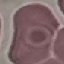
{
  "result": "no malaria parasites detected",
  "capture": "smartphone through the microscope eyepiece",
  "image_type": "cell patch, automatically extracted from a larger field of view and resized to 64 × 64 pixels",
  "preparation": "thin blood smear",
  "stain": "Giemsa"
}